Report the malaria status of this cell.
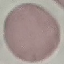
Uninfected.

Summary:
  - Preparation: thin blood smear
  - Capture: smartphone camera at the microscope eyepiece
  - Image type: cell patch, automatically extracted from a larger field of view and resized to 64 × 64 pixels
  - Stain: Giemsa